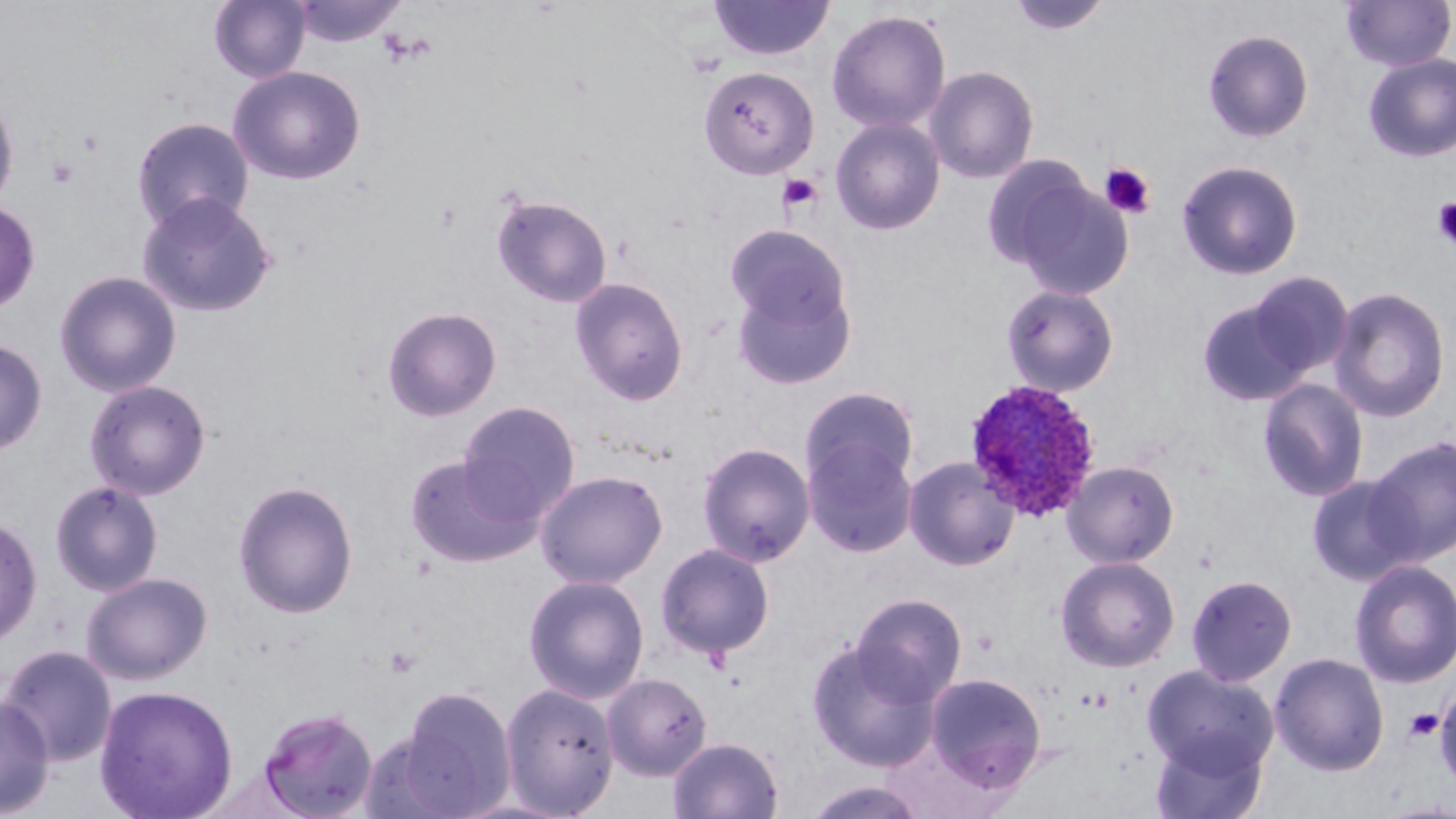

slide-level diagnosis = Plasmodium ovale
preparation = thin blood smear
platelet locations = approximate bounding boxes as (x1,y1)-(x2,y2) corner pairs in pixels: (46,156)-(79,187), (1099,162)-(1157,219), (777,174)-(824,214), (1432,198)-(1456,248), (384,646)-(421,678), (1417,698)-(1452,762), (1404,707)-(1443,744)
modality = light microscopy
magnification = 1000x
image size = 1456×819 pixels
uninfected red blood cell locations = approximate bounding boxes as (x1,y1)-(x2,y2) corner pairs in pixels: (209,0)-(310,84), (291,0)-(408,47), (708,0)-(836,61), (1006,0)-(1112,36), (1342,1)-(1455,71), (826,9)-(951,133), (1203,28)-(1314,143), (1363,54)-(1456,162), (227,65)-(366,185), (698,65)-(820,180), (924,65)-(1039,184), (0,88)-(20,218), (830,116)-(946,235), (131,117)-(254,234), (980,156)-(1095,269), (1176,159)-(1304,281), (1009,179)-(1135,299), (136,191)-(278,319), (492,194)-(612,308), (0,200)-(40,314), (725,224)-(852,337), (54,270)-(182,398), (1247,272)-(1354,379), (731,274)-(856,390), (569,277)-(689,405), (1001,284)-(1120,397), (1329,285)-(1451,423), (1196,298)-(1313,406), (381,306)-(502,421), (0,337)-(48,456), (1257,378)-(1369,502), (84,379)-(212,500), (800,386)-(920,493), (458,401)-(581,520), (1365,435)-(1456,565), (803,438)-(918,557), (697,441)-(816,565), (404,452)-(545,568), (903,455)-(1020,571), (1062,460)-(1179,568), (534,470)-(668,589), (1307,473)-(1422,587), (50,480)-(164,596), (233,480)-(359,618), (0,515)-(42,649), (655,542)-(776,660), (1056,555)-(1180,672), (1349,559)-(1456,689), (82,572)-(213,685), (523,574)-(649,703), (1186,574)-(1297,686), (850,593)-(967,706), (805,640)-(940,771), (0,645)-(117,767), (1270,652)-(1390,776), (1142,665)-(1279,777), (924,672)-(1046,794), (602,673)-(713,781), (499,681)-(619,817), (94,685)-(239,819), (395,686)-(516,817), (1435,686)-(1456,793), (0,693)-(55,816), (256,707)-(379,819), (357,729)-(465,818), (1149,730)-(1269,819), (667,736)-(784,819), (801,779)-(932,819)
field of view = single
Plasmodium ovale-infected red blood cell locations = approximate bounding boxes as (x1,y1)-(x2,y2) corner pairs in pixels: (963,378)-(1101,522)
stain = May-Grünwald-Giemsa